Comment on the morphology of the red blood cells.
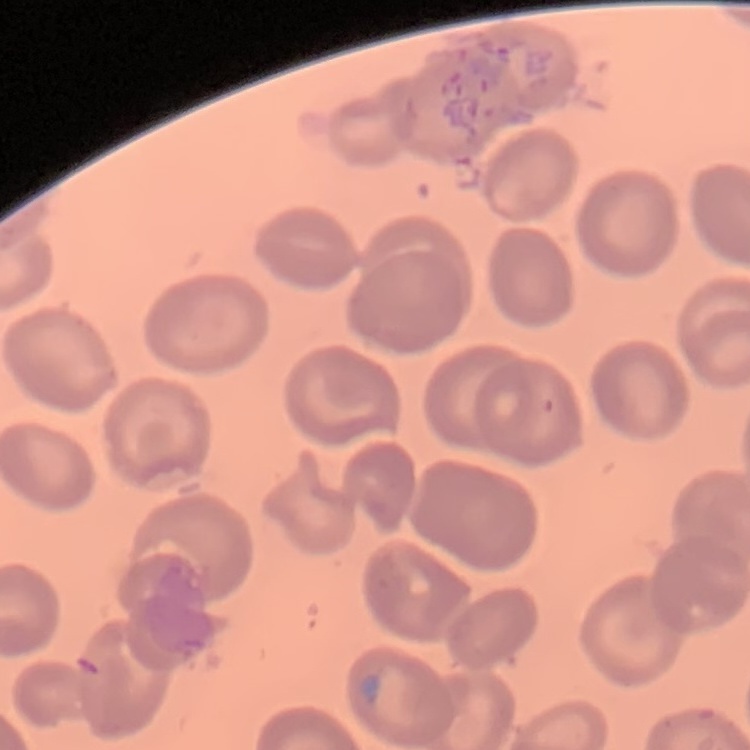

No rouleaux formation.

stain = Field's or Giemsa
preparation = thin blood smear
image type = square crop of a larger photomicrograph